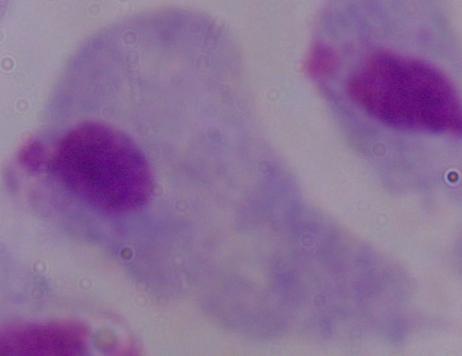
modality: photomicrograph
identification: trichomonad
magnification: 1000x